Locate every Trypanosoma brucei.
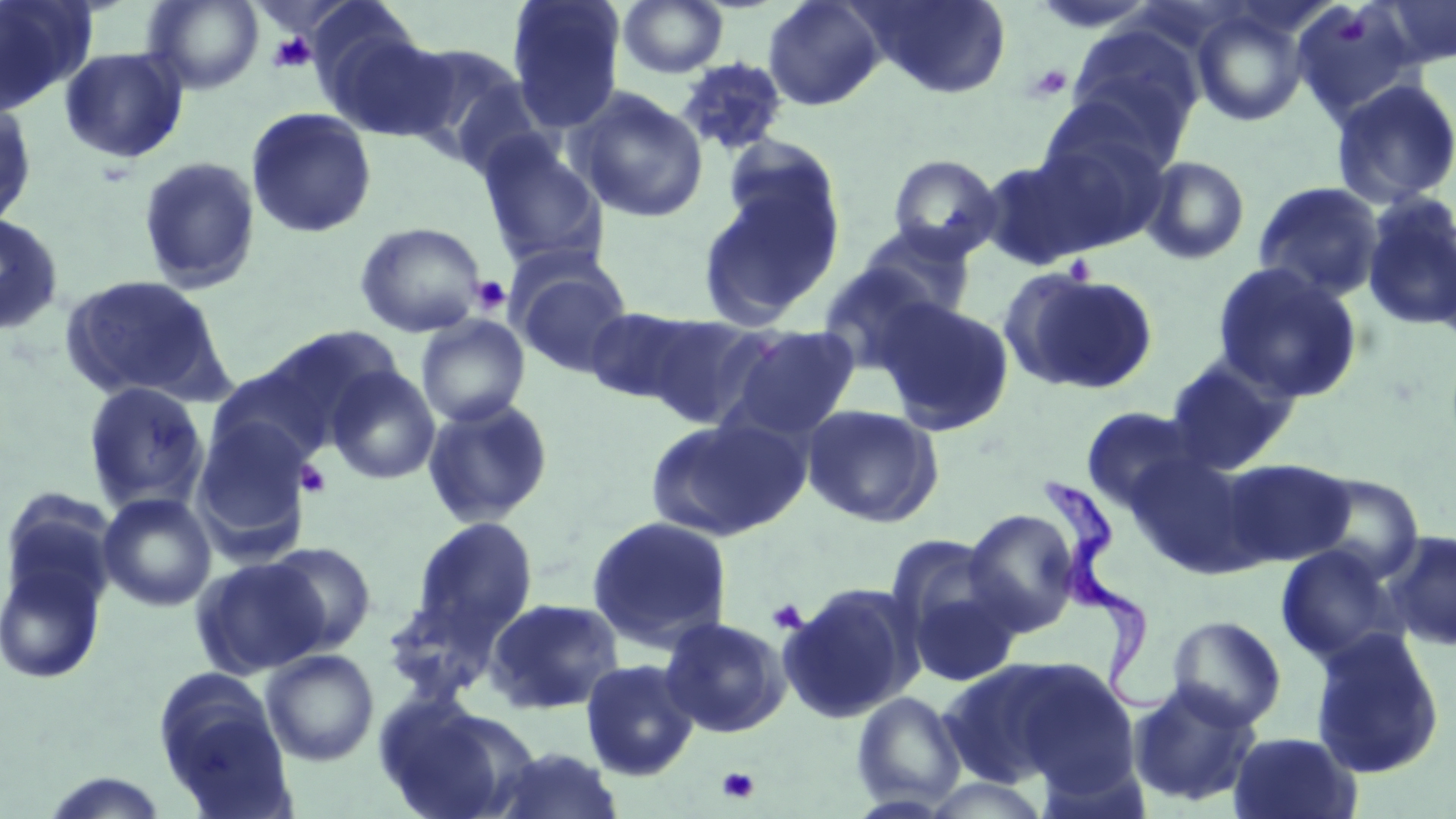

Approximate bounding boxes as (x1, y1, x2, y2) in pixels.
Trypanosoma brucei: (1039, 472, 1169, 712).

Uninfected red blood cell locations: (0, 0, 96, 115), (144, 0, 264, 93), (507, 0, 626, 133), (763, 0, 886, 112), (857, 0, 1011, 98), (1290, 0, 1421, 123), (1374, 0, 1456, 69), (618, 1, 728, 78), (1190, 6, 1312, 127), (314, 16, 452, 142), (1065, 21, 1204, 152), (396, 42, 535, 166), (59, 46, 189, 163), (676, 57, 789, 156), (1329, 78, 1456, 209), (571, 88, 708, 223), (0, 98, 38, 229), (245, 106, 378, 238), (1027, 118, 1174, 250), (475, 133, 608, 271), (888, 154, 1003, 261), (977, 155, 1109, 269), (1140, 155, 1251, 265), (138, 156, 261, 294), (698, 178, 842, 328), (1252, 181, 1384, 302), (1360, 192, 1456, 332), (0, 211, 65, 336), (354, 221, 487, 338), (857, 223, 977, 322), (513, 260, 633, 377), (1211, 260, 1364, 402), (816, 263, 945, 376), (1001, 268, 1160, 395), (60, 275, 228, 403), (876, 298, 1016, 435), (585, 306, 700, 405), (640, 313, 778, 429), (416, 314, 531, 427), (725, 325, 861, 440), (262, 326, 403, 436), (1164, 354, 1299, 473), (206, 365, 331, 471), (326, 365, 440, 485), (81, 381, 211, 513), (422, 397, 555, 528), (802, 404, 944, 527), (1081, 407, 1202, 511), (646, 417, 808, 542), (192, 418, 314, 556), (1124, 452, 1257, 573), (1218, 459, 1355, 567), (1301, 472, 1425, 580), (1, 489, 118, 619), (98, 492, 217, 611), (962, 508, 1083, 635), (585, 515, 734, 651), (410, 516, 538, 649), (1380, 530, 1456, 651), (884, 535, 1009, 652), (265, 541, 377, 653), (1275, 546, 1403, 666), (0, 550, 109, 687), (191, 557, 329, 677), (902, 572, 1025, 688), (780, 581, 922, 723), (382, 588, 502, 704), (485, 597, 625, 715), (1166, 615, 1287, 729), (659, 616, 792, 738), (1310, 628, 1445, 779), (261, 649, 379, 765), (937, 656, 1107, 790), (580, 659, 700, 781), (154, 674, 292, 816), (1126, 680, 1263, 808), (851, 691, 966, 809), (373, 695, 525, 819), (1228, 731, 1361, 819), (483, 746, 627, 819), (920, 776, 1053, 818). Platelet locations: (1336, 12, 1369, 45), (268, 32, 317, 74), (1025, 64, 1071, 102), (1063, 255, 1095, 285), (470, 275, 511, 314), (296, 460, 332, 497), (766, 599, 807, 634), (717, 766, 760, 804). Slide-level diagnosis: Trypanosoma brucei. Single field of view. Thin blood smear. Captured at 1000x magnification. May-Grünwald-Giemsa stain. Image is 1456×819 pixels. Light microscopy.